Outline each blood parasite and name the species.
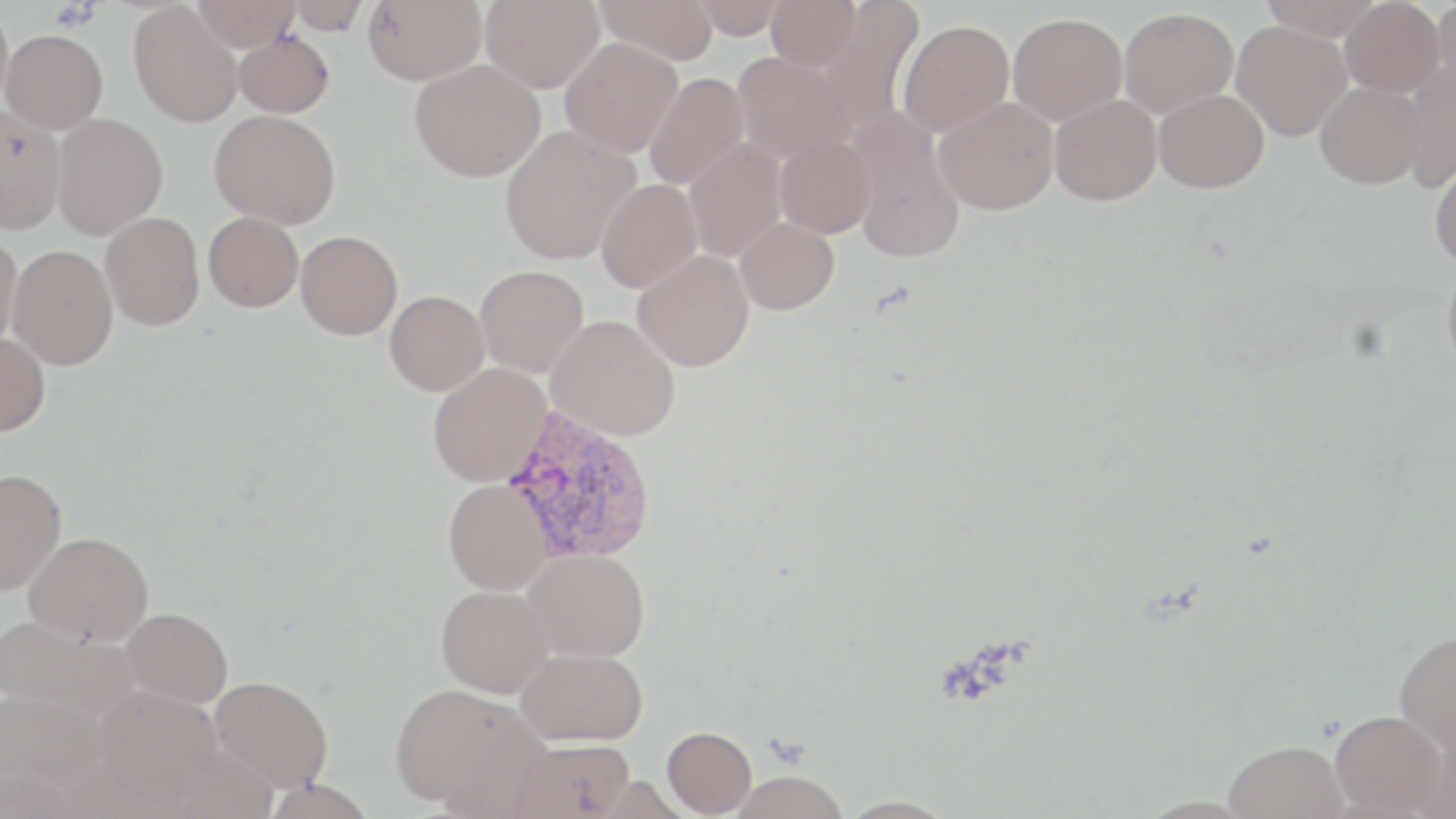

Approximate bounding boxes as [x1, y1, x2, y2] in pixels.
Plasmodium vivax-infected red blood cells: [498, 406, 658, 565].
No Plasmodium falciparum, Plasmodium ovale, Plasmodium malariae, Babesia divergens, or Trypanosoma brucei observed.

slide-level diagnosis = Plasmodium vivax
platelet locations = approximate bounding boxes as [x1, y1, x2, y2] in pixels: [50, 2, 100, 31]
preparation = thin blood smear
stain = May-Grünwald-Giemsa
uninfected red blood cell locations = approximate bounding boxes as [x1, y1, x2, y2] in pixels: [193, 0, 301, 50], [284, 0, 371, 34], [363, 0, 487, 85], [480, 0, 604, 92], [595, 0, 720, 64], [688, 0, 790, 39], [765, 0, 862, 71], [813, 0, 926, 135], [1259, 0, 1384, 40], [1339, 0, 1445, 96], [1430, 0, 1456, 97], [0, 2, 13, 117], [129, 3, 243, 127], [1119, 7, 1238, 118], [1008, 13, 1127, 125], [897, 20, 1014, 137], [1231, 21, 1352, 141], [1, 29, 108, 134], [234, 32, 334, 118], [560, 37, 683, 158], [732, 51, 853, 164], [409, 60, 545, 182], [1397, 64, 1456, 193], [644, 72, 751, 190], [1315, 80, 1426, 189], [1153, 89, 1269, 192], [1050, 94, 1162, 206], [934, 97, 1058, 215], [0, 105, 67, 234], [210, 109, 340, 228], [846, 111, 966, 263], [51, 113, 168, 239], [499, 126, 640, 264], [775, 133, 877, 238], [682, 138, 787, 261], [1429, 158, 1456, 269], [596, 179, 702, 292], [101, 212, 204, 330], [203, 212, 303, 312], [735, 217, 839, 315], [296, 231, 403, 339], [0, 233, 22, 351], [7, 243, 118, 369], [632, 249, 754, 371], [1442, 257, 1456, 380], [475, 265, 589, 377], [385, 291, 489, 395], [546, 315, 680, 441], [0, 333, 50, 435], [428, 363, 551, 486], [0, 469, 66, 595], [444, 479, 554, 594], [23, 532, 153, 645], [523, 548, 650, 662], [436, 584, 553, 697], [122, 607, 232, 707], [0, 614, 139, 720], [1394, 628, 1456, 758], [516, 646, 647, 745], [210, 675, 333, 792], [390, 684, 528, 806], [94, 686, 223, 807], [1330, 710, 1447, 817], [662, 726, 757, 816], [513, 739, 635, 819], [1224, 741, 1349, 819], [729, 770, 847, 818], [0, 772, 76, 818], [836, 796, 959, 819]
field of view = one of a larger specimen
modality = light microscopy
image size = 1456×819 pixels
magnification = 1000x